Classify this cell by malaria status.
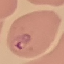

Parasitized.

{
  "preparation": "thin blood smear",
  "capture": "smartphone camera at the microscope eyepiece",
  "image_type": "cell patch, automatically extracted from a larger field of view and resized to 64 × 64 pixels",
  "stain": "Giemsa"
}